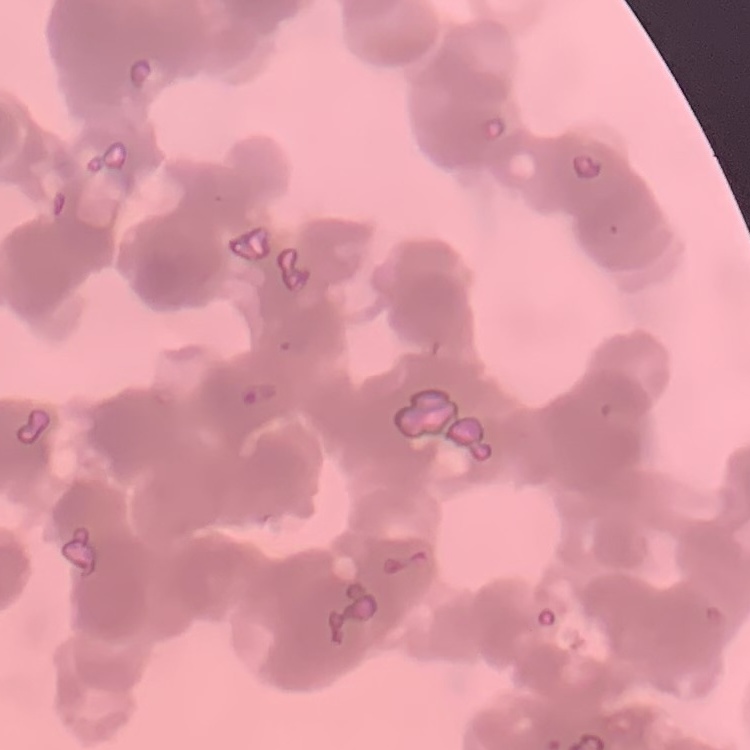
Summary:
  - Erythrocyte morphology: rouleaux formation
  - Image type: square crop of a larger photomicrograph
  - Stain: Field's or Giemsa
  - Preparation: thin blood smear